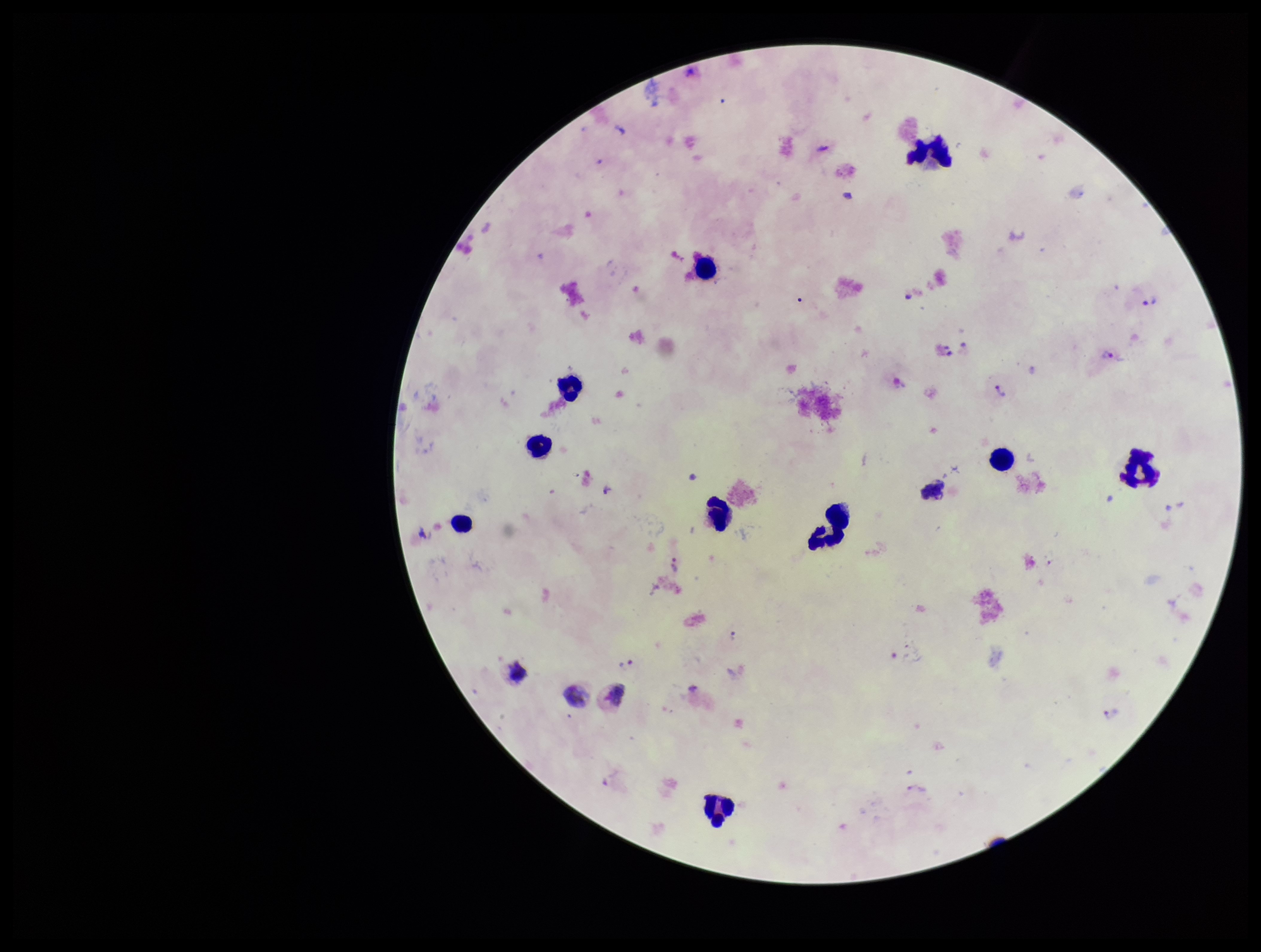

species reported for this patient = Plasmodium vivax
Plasmodium parasites = identified
stain = Giemsa
capture = smartphone photograph through the microscope eyepiece
field of view = one from this slide
patient malaria status = positive
leukocyte count = 14
image size = 1261×952 pixels
parasite count = 7
preparation = thick blood smear